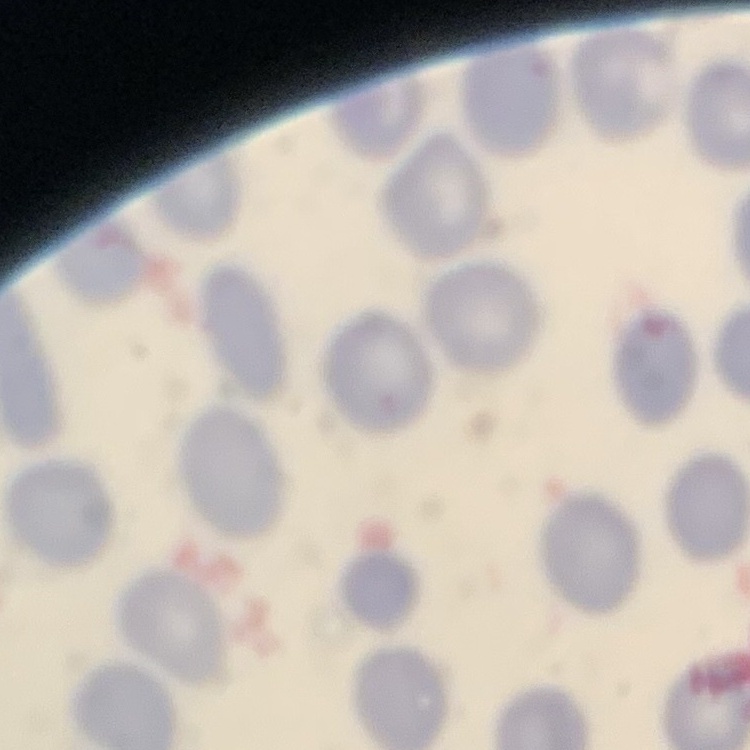 The red blood cells exhibit no rouleaux formation. Field's or Giemsa stain. Thin blood smear. One tile cut from a larger photomicrograph.